Name the blood parasite species.
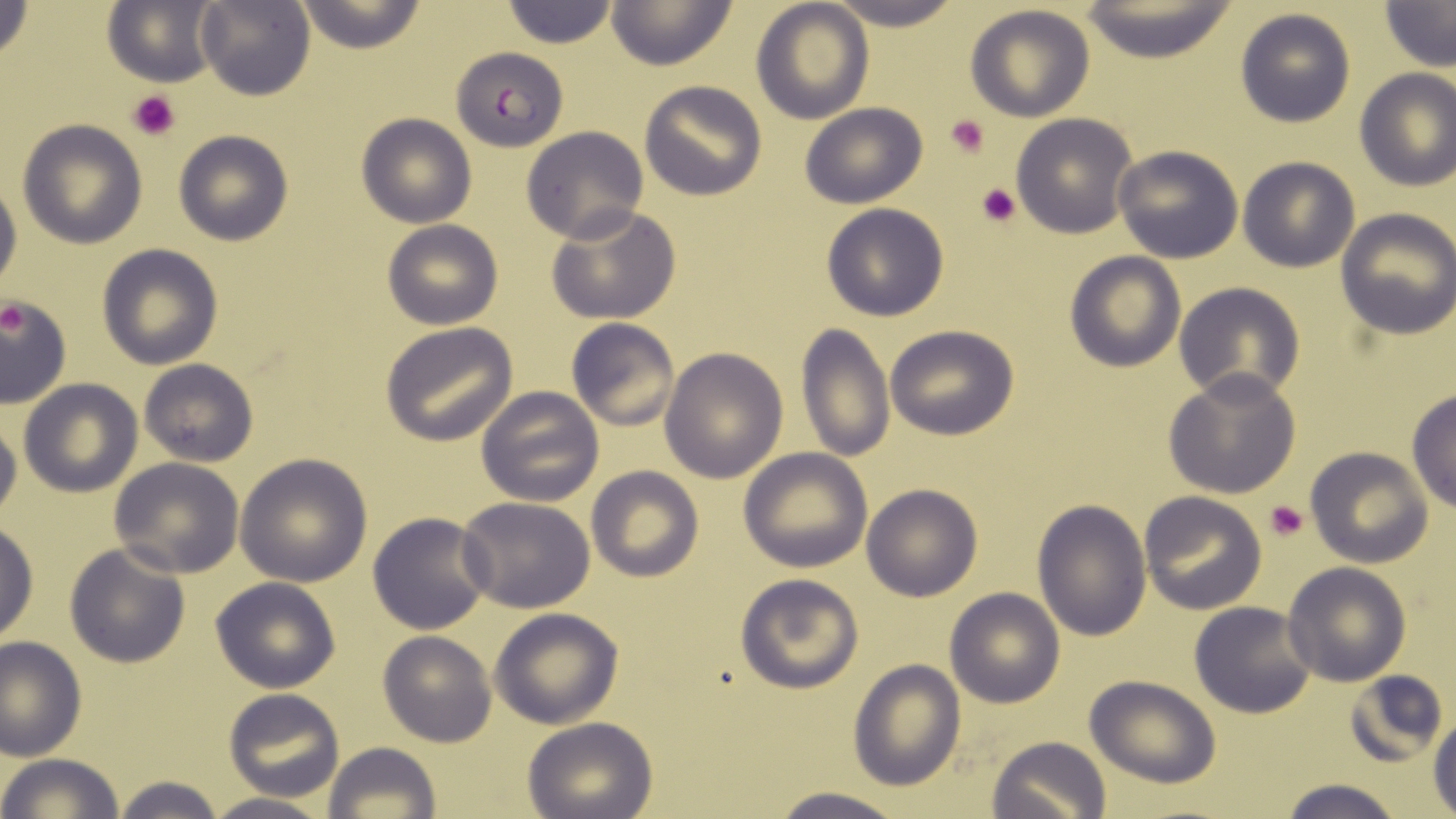
Plasmodium falciparum.

modality = light microscopy
preparation = thin blood film
field of view = one of a larger specimen
platelet locations = approximate bounding boxes as [x1, y1, x2, y2] in pixels: [129, 89, 182, 141], [945, 114, 992, 160], [975, 183, 1021, 228], [1, 306, 34, 342], [1264, 498, 1310, 541]
stain = May-Grünwald-Giemsa
magnification = 1000x
image size = 1456×819 pixels
Plasmodium falciparum-infected red blood cell locations = approximate bounding boxes as [x1, y1, x2, y2] in pixels: [450, 46, 568, 151]
uninfected red blood cell locations = approximate bounding boxes as [x1, y1, x2, y2] in pixels: [0, 0, 34, 65], [196, 0, 314, 102], [502, 0, 618, 49], [604, 0, 737, 70], [750, 0, 873, 122], [822, 0, 969, 29], [292, 1, 428, 52], [1378, 1, 1456, 70], [102, 2, 221, 87], [1074, 2, 1242, 63], [964, 5, 1096, 122], [1233, 8, 1356, 128], [1353, 68, 1456, 191], [639, 81, 767, 201], [798, 103, 927, 209], [357, 112, 476, 228], [1010, 113, 1139, 238], [17, 120, 147, 248], [522, 126, 649, 245], [173, 130, 293, 245], [1112, 144, 1243, 263], [1237, 157, 1360, 272], [0, 172, 21, 301], [545, 203, 683, 326], [820, 203, 950, 321], [1334, 209, 1456, 339], [381, 218, 503, 330], [96, 243, 223, 369], [1064, 251, 1187, 373], [1174, 282, 1306, 405], [0, 295, 71, 408], [567, 318, 681, 433], [381, 323, 517, 446], [796, 324, 894, 465], [884, 324, 1020, 440], [659, 347, 787, 483], [139, 358, 258, 466], [1162, 370, 1302, 499], [18, 378, 142, 496], [476, 384, 605, 508], [1407, 391, 1456, 513], [0, 407, 21, 520], [1305, 447, 1434, 567], [738, 448, 873, 572], [235, 455, 372, 586], [107, 457, 244, 576], [586, 466, 703, 581], [862, 483, 981, 600], [1139, 492, 1267, 613], [457, 496, 595, 612], [1033, 499, 1152, 642], [368, 510, 493, 633], [0, 521, 38, 645], [66, 543, 189, 668], [1282, 562, 1411, 685], [734, 572, 867, 694], [210, 576, 340, 693], [944, 587, 1066, 709], [1189, 602, 1317, 718], [489, 608, 624, 729], [378, 631, 498, 746], [0, 635, 86, 761], [847, 658, 965, 792], [1345, 670, 1450, 768], [1084, 675, 1223, 787], [222, 689, 345, 801], [1429, 716, 1456, 816], [523, 717, 658, 819], [987, 736, 1111, 819], [323, 742, 439, 819], [0, 753, 126, 819], [108, 775, 228, 819], [1276, 778, 1407, 819], [767, 788, 908, 819], [200, 792, 335, 819]